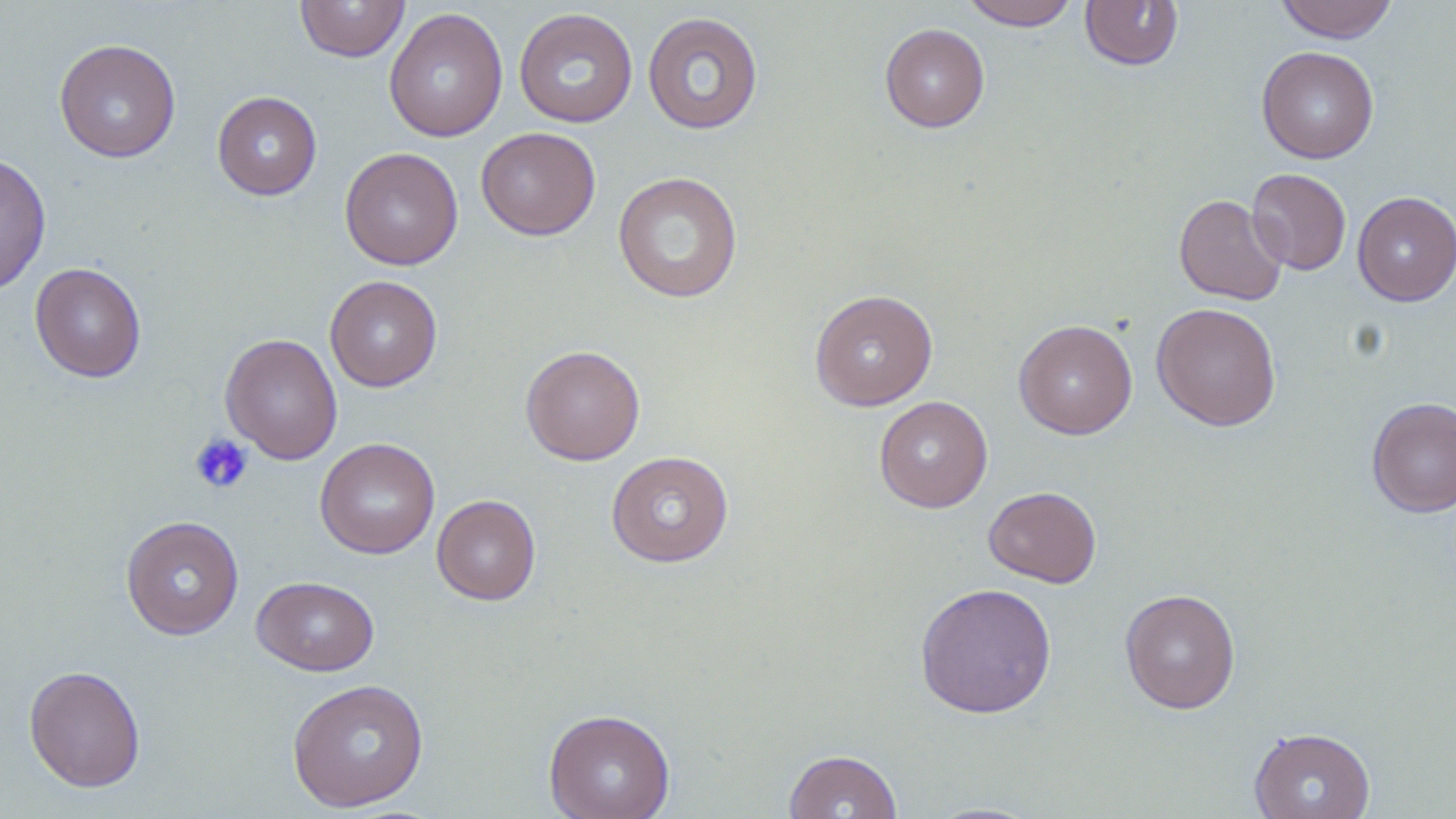 Approximate bounding boxes as (x1,y1)-(x2,y2) corner pairs in pixels. Uninfected red blood cell locations: (295,0)-(410,62), (961,0)-(1079,30), (1080,0)-(1184,71), (1274,0)-(1399,43), (383,7)-(508,142), (514,8)-(638,128), (642,11)-(763,135), (879,23)-(990,133), (54,39)-(181,163), (1257,45)-(1379,164), (212,91)-(322,200), (476,127)-(601,241), (340,147)-(463,270), (0,154)-(52,296), (1247,168)-(1351,275), (612,171)-(744,304), (1352,191)-(1456,306), (1173,194)-(1288,306), (29,262)-(146,382), (325,275)-(442,392), (809,289)-(938,411), (1152,302)-(1282,431), (1013,319)-(1138,439), (220,333)-(342,465), (520,344)-(646,466), (873,395)-(993,513), (1367,396)-(1456,517), (315,438)-(440,559), (606,450)-(734,568), (983,485)-(1102,588), (432,494)-(541,605), (121,515)-(244,640), (252,575)-(379,676), (915,582)-(1057,718), (1119,588)-(1240,714), (23,664)-(146,793), (286,678)-(429,812), (543,708)-(675,819), (1249,727)-(1376,819), (784,749)-(903,819), (922,801)-(1046,818). Platelet locations: (189,433)-(254,494). Slide-level diagnosis: negative for blood parasites. 1000x magnification. Thin blood smear. May-Grünwald-Giemsa-stained preparation. Light microscopy. Image is 1456×819 pixels. One field of a larger specimen.